Name the parasite shown.
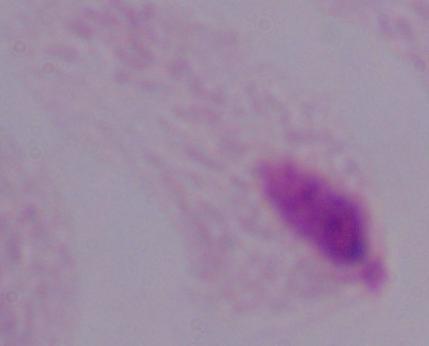
A trichomonad.

modality: photomicrograph
magnification: 1000x